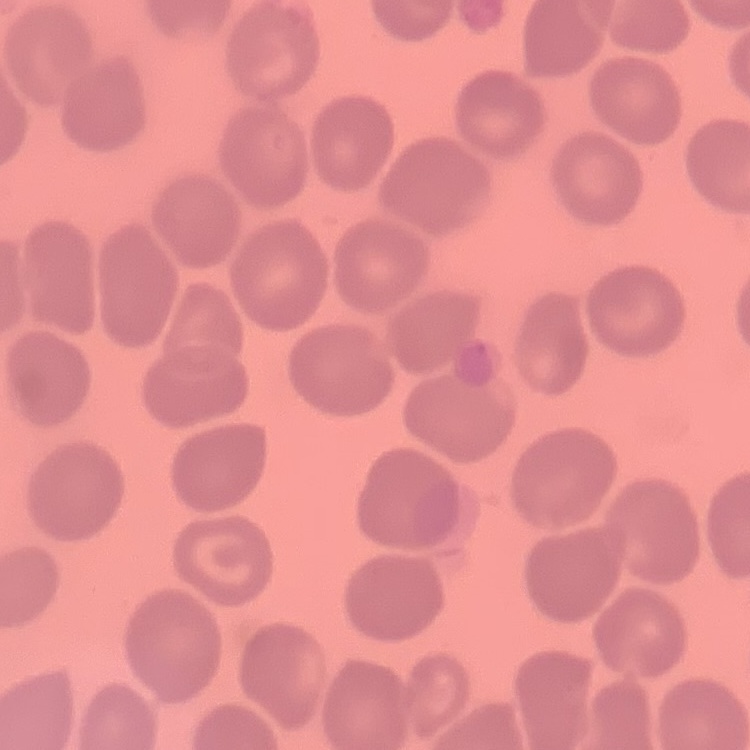
{
  "red_blood_cell_morphology": "no rouleaux formation",
  "image_type": "one tile cut from a larger photomicrograph",
  "stain": "Field's or Giemsa",
  "preparation": "thin peripheral smear"
}